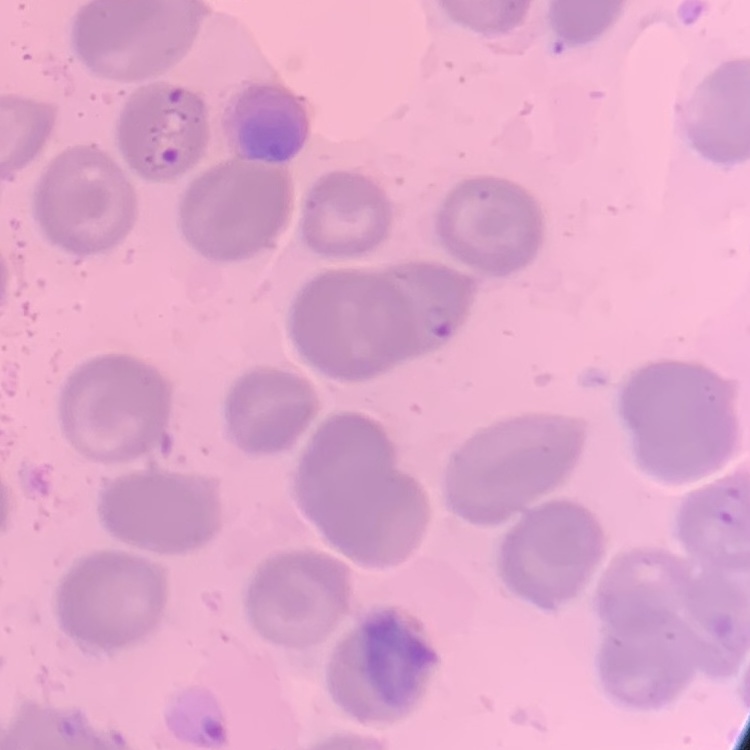

red_blood_cell_morphology: no rouleaux formation
stain: Field's or Giemsa
preparation: thin blood smear
image_type: square crop of a larger photomicrograph